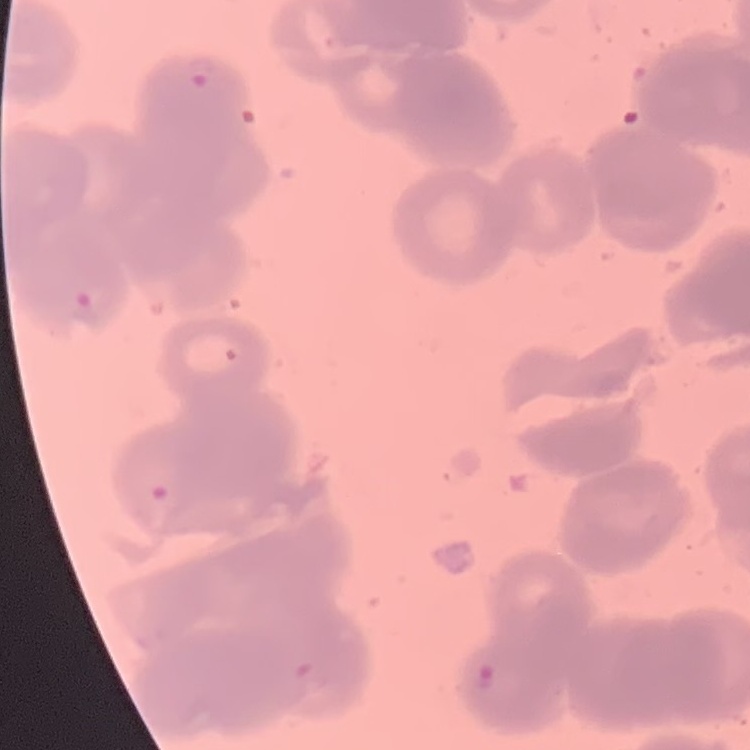

red blood cell morphology = rouleaux formation
image type = one tile cut from a larger photomicrograph
stain = Field's or Giemsa
preparation = thin blood smear